Identify the cell.
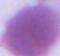

An erythrocyte.

Summary:
  - Magnification: 1000x
  - Modality: photomicrograph